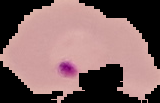

{
  "preparation": "thin blood smear",
  "image_type": "segmented cell region with the area outside set to black",
  "malaria_status": "parasitized",
  "image_size": "160×103 pixels"
}